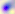
modality: micrograph
identification: Toxoplasma gondii
magnification: 400x